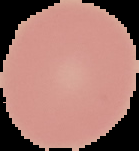

preparation = thin blood film
result = no Plasmodium parasites seen
image type = segmented cell region with the area outside set to black
image size = 139×151 pixels